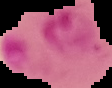
From a thin blood film. The area outside the segmented cell region is set to black. Malaria status: parasitized. Image is 112×88 pixels.